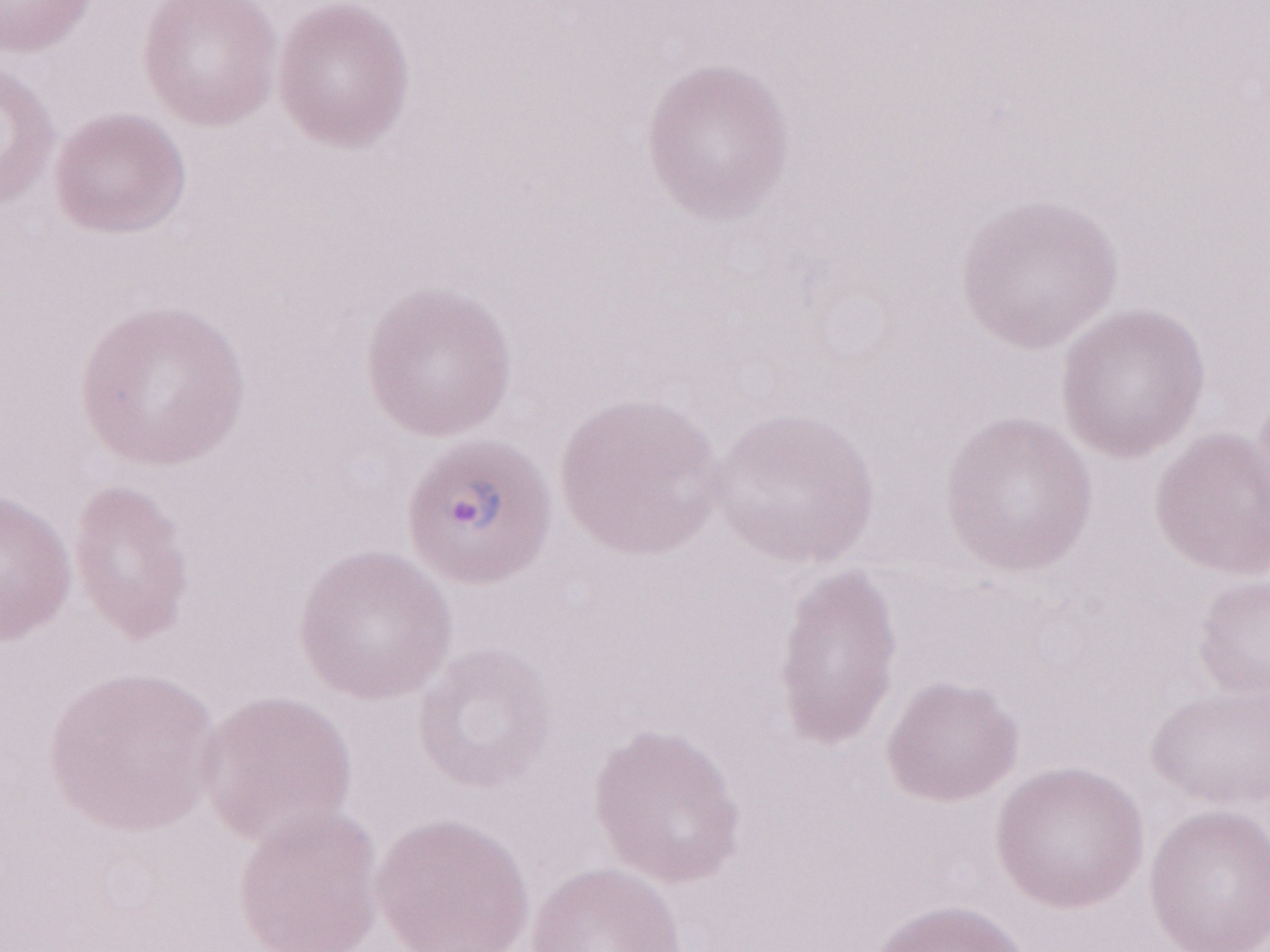 Patient-level malaria diagnosis: positive. Magnification: 1,000x. Single field of view. Olympus BX43 microscope, Olympus DP73 camera. Image is 1270×952 pixels. Thin peripheral-blood smear. May-Grünwald-Giemsa stain.